Give the position of every leukocyte visible.
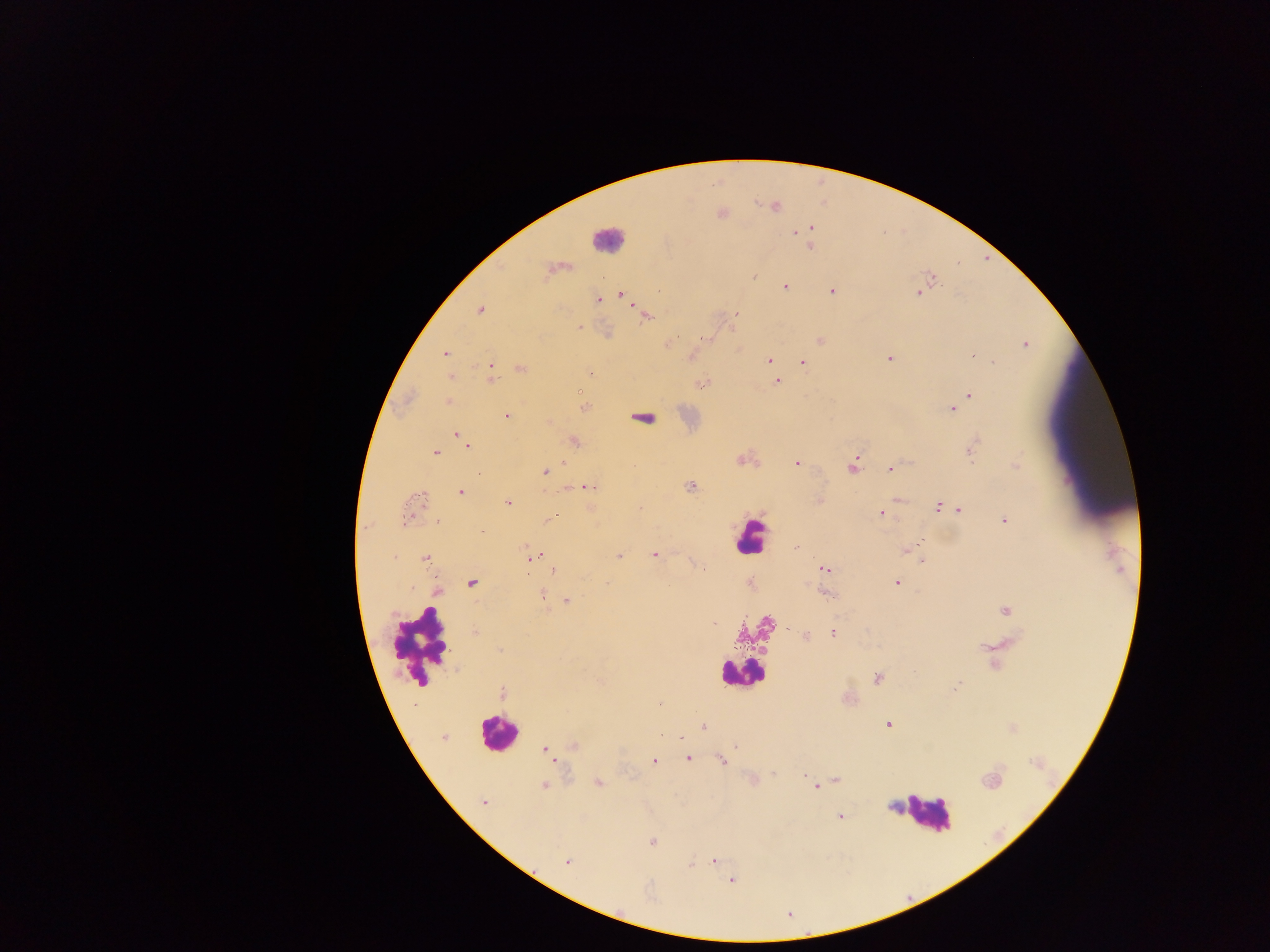
Approximate centers as (x, y) in pixels.
Leukocytes: (608, 239), (749, 536), (419, 645), (742, 674), (497, 733), (925, 813).

{
  "capture": "mobile-phone photograph through a microscope",
  "field_of_view": "single",
  "preparation": "thick blood smear",
  "country": "Ghana",
  "image_size": "1270×952 pixels",
  "plasmodium_parasite_locations": "approximate centers as (x, y) in pixels: (776, 206), (811, 228), (796, 233), (810, 246), (548, 270), (754, 276), (932, 278), (785, 286), (832, 291), (918, 292), (623, 295), (598, 300), (479, 310), (736, 314), (647, 316), (580, 326), (703, 339), (820, 340), (668, 344), (1025, 344), (445, 354), (972, 355), (889, 358), (769, 360), (802, 362), (992, 362), (771, 364), (491, 368), (521, 368), (589, 373), (492, 375), (450, 377), (777, 382), (701, 385), (579, 391), (970, 395), (448, 402), (584, 407), (952, 409), (506, 416), (642, 419), (549, 421), (457, 434), (461, 437), (576, 442), (467, 445), (435, 452), (970, 452), (741, 460), (796, 463), (1016, 465), (852, 466), (891, 469), (545, 472), (690, 486), (586, 487), (460, 492), (508, 502), (939, 506), (958, 510), (882, 513), (407, 514), (552, 517), (437, 520), (1004, 520), (917, 546), (795, 547), (905, 551), (653, 555), (394, 556), (535, 556), (619, 557), (426, 559), (921, 560), (553, 569), (824, 569), (897, 582), (471, 583), (542, 595), (828, 595), (567, 600), (1006, 611), (714, 624), (833, 634), (805, 635), (877, 678), (956, 687), (502, 693), (887, 724), (704, 727), (661, 736), (444, 738), (574, 746), (736, 746), (545, 750), (689, 759), (722, 761), (653, 762), (804, 775), (836, 780), (991, 781), (599, 783), (544, 786), (816, 786), (484, 802), (840, 816), (652, 842), (714, 861), (567, 862), (689, 865), (731, 881)"
}